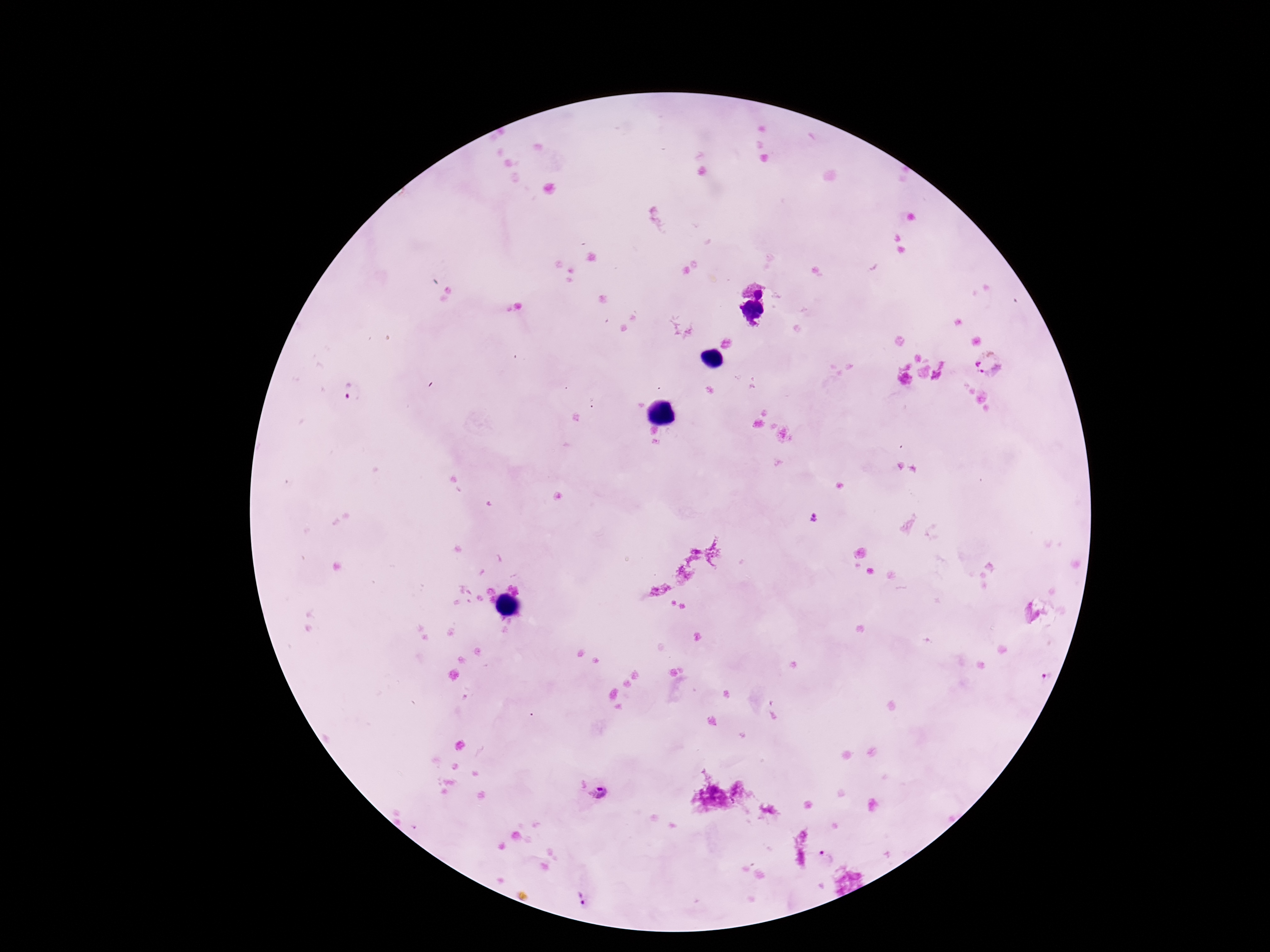
Approximate centers as [x, y] in pixels.
Summary:
  - Plasmodium parasite locations: [758, 287], [754, 312], [988, 365], [352, 390], [812, 516], [1046, 677], [599, 793], [824, 858], [581, 899]
  - Patient malaria status: positive
  - Magnification: 100x
  - Field of view: single
  - Capture: smartphone camera through the microscope eyepiece
  - Stain: Giemsa
  - Image size: 1270×952 pixels
  - Preparation: thick blood film